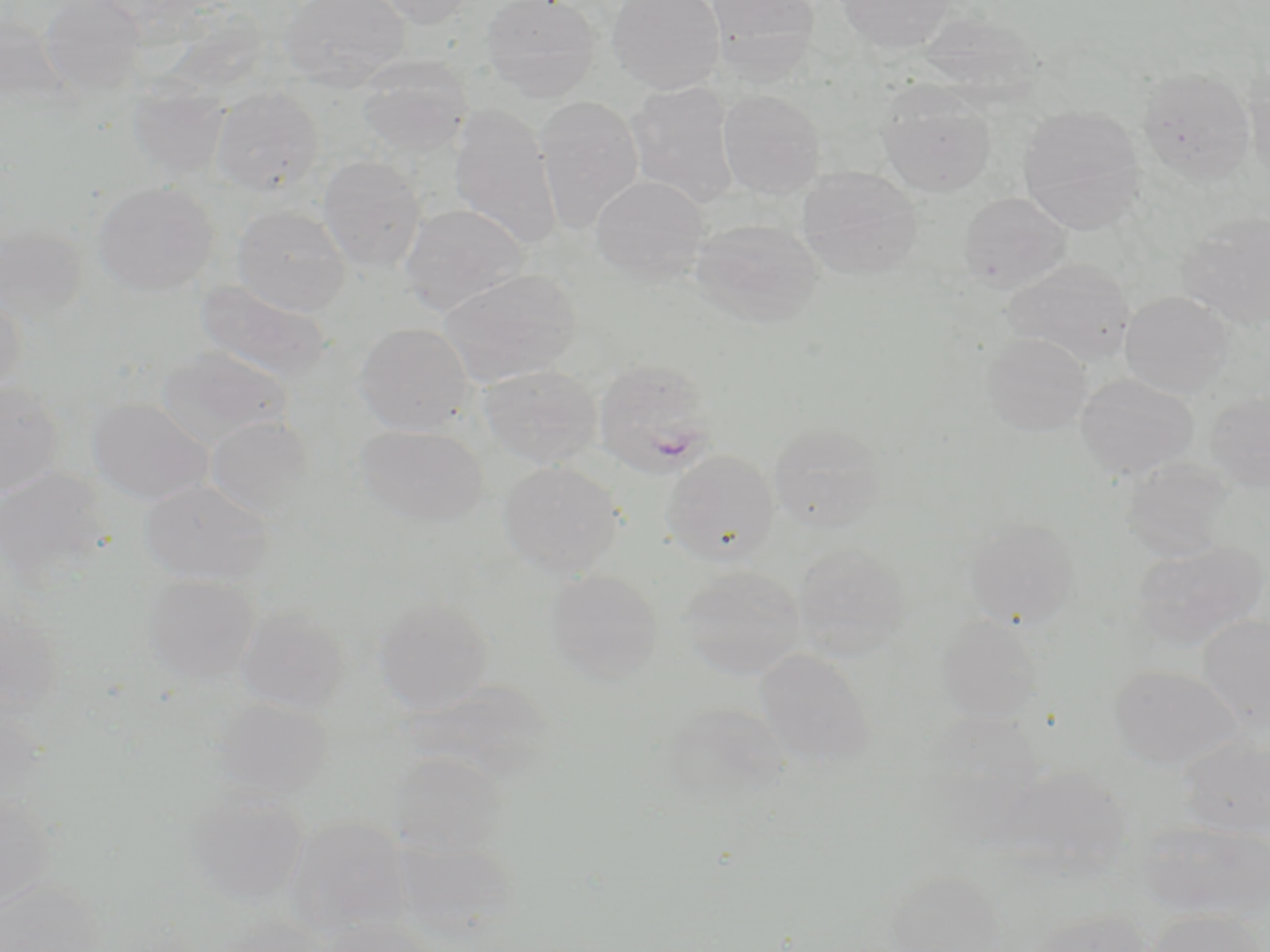

slide_level_diagnosis: Plasmodium ovale
magnification: 1000x
plasmodium_ovale_infected_red_blood_cell_locations: 'approximate bounding boxes as [x1, y1, x2, y2] in pixels: [593, 358, 720, 479]'
stain: May-Grünwald-Giemsa
image_size: 1270×952 pixels
uninfected_red_blood_cell_locations: 'approximate bounding boxes as [x1, y1, x2, y2] in pixels: [39, 0, 146, 98], [278, 0, 411, 91], [366, 0, 475, 28], [480, 0, 601, 102], [607, 0, 725, 94], [705, 0, 820, 82], [837, 0, 954, 52], [920, 12, 1041, 103], [356, 55, 471, 157], [1137, 67, 1257, 184], [1245, 71, 1270, 188], [127, 78, 231, 181], [626, 81, 739, 207], [877, 83, 996, 198], [211, 85, 325, 195], [717, 89, 826, 198], [534, 94, 644, 234], [448, 104, 561, 250], [1019, 104, 1145, 234], [318, 155, 426, 272], [797, 166, 922, 279], [590, 174, 711, 285], [92, 181, 218, 297], [958, 191, 1071, 291], [400, 203, 530, 315], [232, 205, 351, 316], [1177, 212, 1270, 331], [688, 216, 825, 328], [1, 224, 88, 327], [1002, 258, 1136, 364], [436, 268, 581, 385], [195, 279, 334, 383], [0, 290, 27, 396], [1119, 291, 1234, 398], [354, 322, 474, 435], [981, 332, 1092, 436], [157, 346, 293, 447], [478, 363, 603, 468], [1075, 373, 1199, 480], [0, 379, 66, 498], [1206, 389, 1270, 492], [87, 398, 213, 505], [205, 415, 316, 519], [768, 419, 888, 534], [354, 424, 489, 528], [662, 449, 780, 566], [1121, 457, 1233, 561], [499, 460, 625, 577], [0, 467, 111, 587], [139, 479, 274, 585], [964, 518, 1079, 629], [1130, 539, 1266, 651], [792, 541, 911, 659], [679, 566, 805, 679], [543, 568, 664, 684], [142, 574, 260, 683], [372, 596, 493, 714], [0, 603, 66, 718], [234, 605, 350, 714], [1198, 614, 1270, 726], [937, 615, 1047, 724], [756, 648, 875, 768], [1109, 664, 1241, 772], [409, 680, 560, 784], [211, 698, 335, 800], [0, 701, 48, 813], [661, 703, 789, 806], [918, 710, 1046, 832], [1179, 734, 1270, 839], [388, 752, 509, 858], [991, 764, 1132, 878], [183, 789, 308, 908], [0, 794, 56, 911], [284, 815, 412, 937], [1136, 820, 1270, 921], [393, 837, 519, 936], [887, 872, 1006, 952], [0, 877, 106, 952], [1029, 908, 1152, 952], [1146, 908, 1264, 952], [203, 915, 332, 952], [316, 918, 439, 952]'
preparation: thin blood smear
field_of_view: single
modality: optical microscopy